Point out each malaria parasite and each leukocyte.
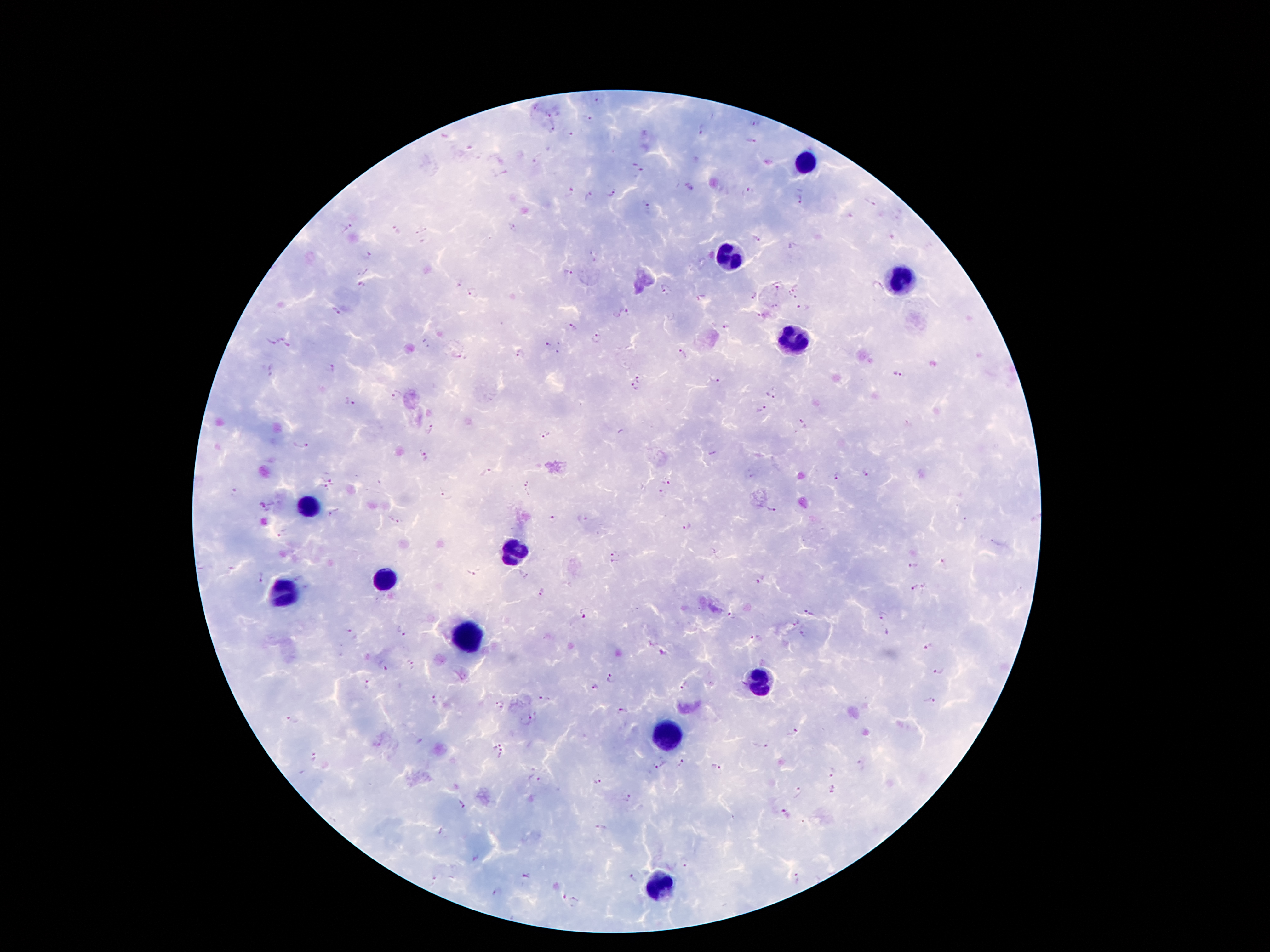

Approximate centers as (x, y) in pixels.
Malaria parasites: (596, 101), (537, 107), (549, 114), (587, 117), (756, 124), (702, 128), (553, 130), (751, 141), (538, 160), (637, 168), (750, 191), (569, 192), (611, 192), (588, 196), (798, 199), (872, 200), (645, 203), (512, 226), (348, 227), (396, 231), (757, 238), (593, 255), (369, 256), (568, 273), (459, 282), (776, 282), (361, 285), (666, 290), (473, 293), (794, 294), (752, 295), (775, 307), (803, 308), (335, 312), (627, 312), (758, 315), (573, 326), (726, 328), (598, 339), (287, 342), (269, 343), (427, 344), (550, 345), (684, 353), (519, 356), (333, 368), (272, 371), (901, 374), (639, 376), (714, 380), (632, 388), (771, 394), (395, 395), (350, 403), (761, 410), (804, 425), (431, 428), (545, 432), (302, 443), (424, 457), (487, 471), (866, 472), (328, 475), (837, 478), (666, 482), (323, 489), (528, 490), (237, 491), (659, 491), (444, 494), (263, 507), (771, 510), (336, 513), (392, 520), (554, 520), (583, 520), (687, 526), (283, 533), (614, 558), (942, 564), (915, 567), (473, 573), (523, 574), (258, 577), (761, 579), (926, 585), (915, 589), (540, 595), (810, 610), (583, 616), (731, 616), (884, 616), (793, 619), (402, 632), (352, 634), (804, 635), (755, 636), (927, 646), (412, 664), (384, 665), (940, 672), (610, 678), (684, 683), (367, 685), (595, 688), (434, 699), (543, 700), (929, 700), (499, 705), (623, 712), (292, 720), (528, 720), (790, 731), (496, 742), (765, 746), (502, 755), (313, 757), (660, 764), (683, 764), (716, 767), (861, 767), (832, 772), (599, 780), (535, 781), (834, 790), (796, 794), (629, 798), (462, 804), (785, 813), (600, 829), (440, 831), (687, 866), (526, 876), (797, 877), (630, 879), (495, 893), (576, 903).
Leukocytes: (805, 163), (730, 256), (898, 279), (795, 337), (304, 508), (507, 550), (381, 582), (284, 592), (472, 631), (756, 679), (669, 737), (659, 889).

preparation = thick blood smear
stain = Giemsa
capture = smartphone through the microscope eyepiece
patient malaria status = infected with Plasmodium falciparum
image size = 1270×952 pixels
magnification = 100x
field of view = one from this slide